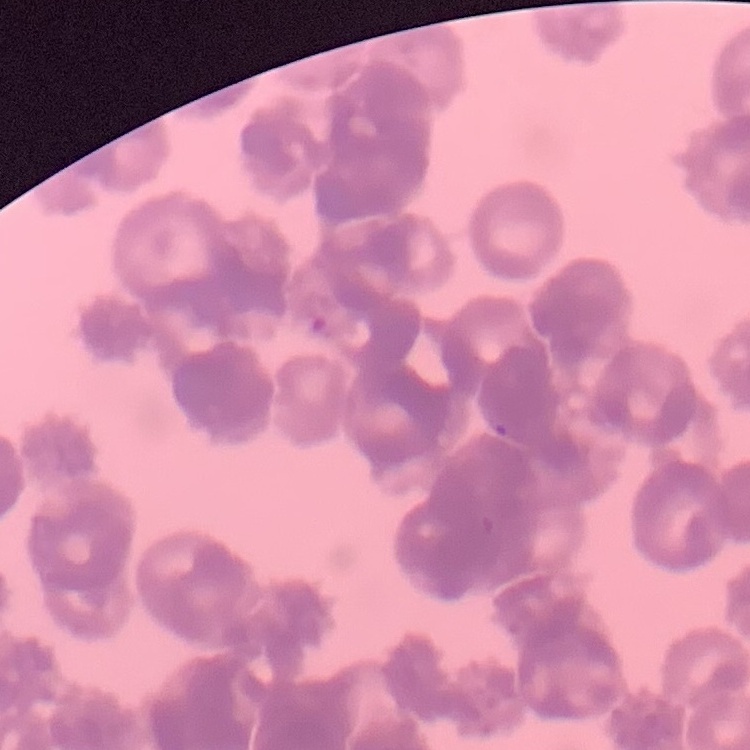 The red blood cells exhibit rouleaux formation. Field's or Giemsa stain. Square crop of a larger photomicrograph. Thin blood film.